State which parasite is depicted.
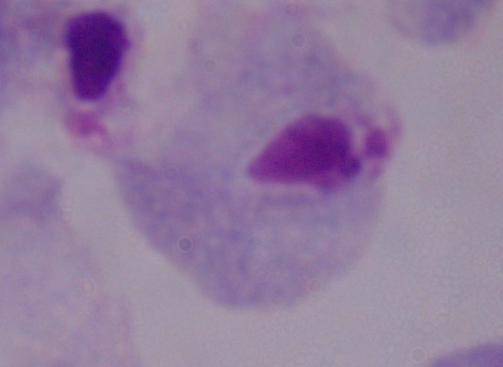

A trichomonad.

Micrograph. 1000x magnification.